Name the parasite shown.
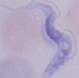
A trypanosome.

Summary:
  - Modality: photomicrograph
  - Magnification: 1000x